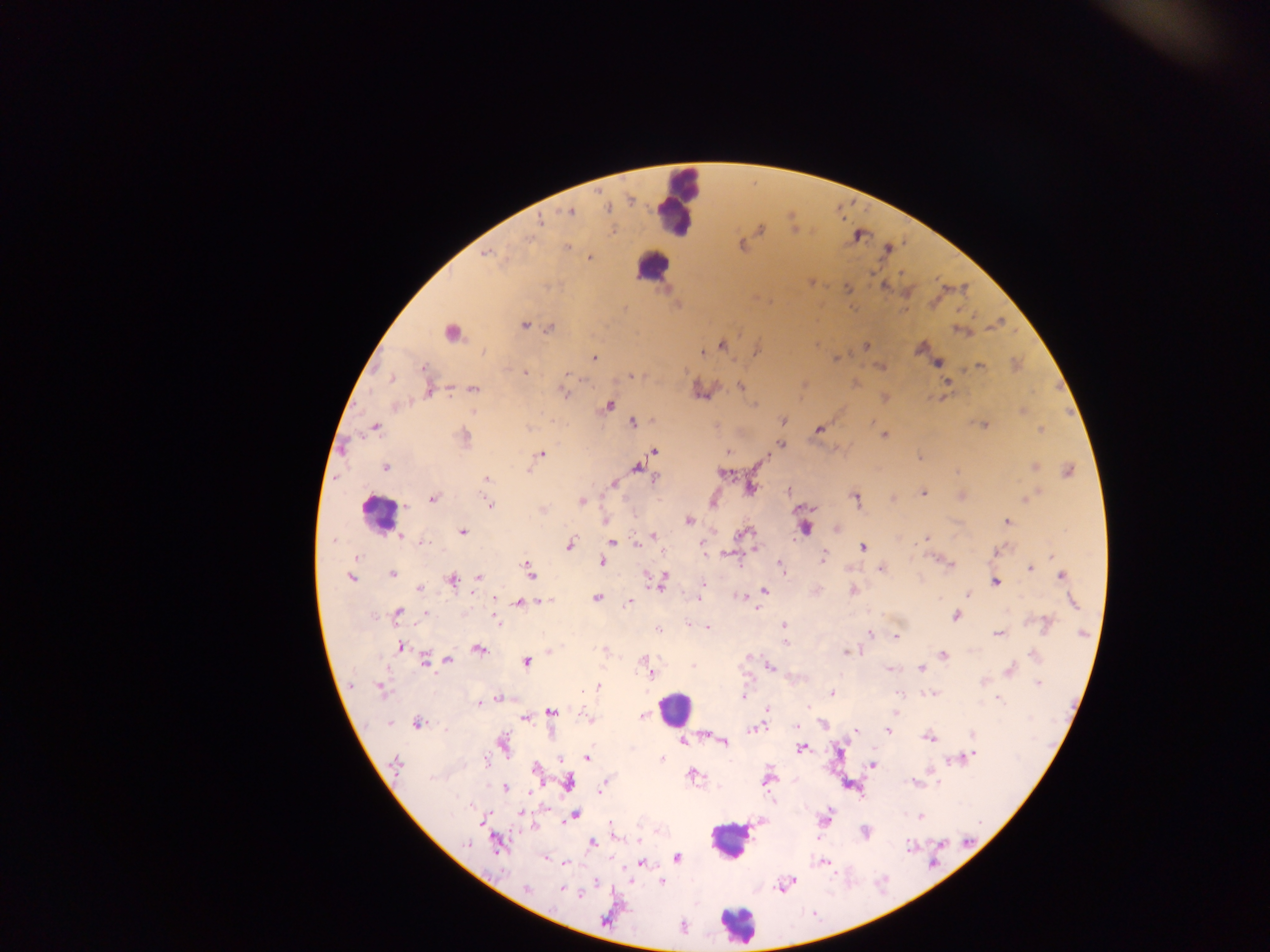
Approximate centers as [x, y] in pixels.
Summary:
  - Malaria parasite locations: [569, 212], [540, 220], [759, 229], [613, 230], [741, 245], [567, 247], [487, 255], [589, 258], [810, 282], [883, 285], [847, 288], [963, 289], [524, 325], [995, 325], [549, 328], [961, 331], [452, 332], [721, 344], [866, 346], [920, 347], [756, 351], [700, 353], [593, 358], [835, 358], [937, 363], [1014, 365], [880, 366], [979, 367], [524, 373], [630, 375], [391, 378], [804, 384], [854, 384], [947, 384], [741, 386], [428, 388], [473, 389], [563, 392], [884, 398], [397, 405], [608, 406], [1022, 410], [782, 421], [633, 422], [983, 425], [374, 426], [818, 430], [1040, 430], [884, 435], [463, 438], [780, 445], [652, 450], [727, 451], [540, 454], [920, 456], [645, 458], [1033, 466], [386, 467], [636, 467], [528, 470], [1068, 471], [723, 473], [486, 479], [655, 479], [613, 483], [749, 488], [789, 490], [922, 492], [962, 496], [855, 497], [432, 498], [892, 498], [1026, 498], [581, 501], [711, 501], [488, 504], [542, 510], [606, 519], [687, 520], [1006, 522], [804, 526], [837, 528], [462, 532], [744, 532], [654, 536], [399, 537], [926, 537], [612, 542], [423, 543], [569, 544], [637, 544], [703, 546], [862, 547], [996, 550], [729, 553], [822, 557], [1051, 557], [355, 558], [942, 561], [602, 562], [780, 568], [881, 568], [1029, 568], [529, 570], [392, 574], [1061, 575], [351, 577], [479, 577], [648, 577], [451, 580], [662, 580], [995, 581], [703, 583], [418, 588], [764, 590], [853, 590], [968, 593], [741, 596], [597, 598], [495, 599], [698, 599], [542, 600], [628, 601], [519, 602], [1072, 602], [759, 608], [397, 613], [425, 614], [955, 615], [495, 617], [1046, 623], [688, 624], [782, 624], [657, 629], [708, 629], [869, 633], [998, 633], [895, 637], [785, 642], [399, 646], [478, 649], [605, 650], [549, 651], [846, 651], [943, 654], [446, 659], [426, 660], [526, 662], [646, 663], [769, 666], [920, 668], [889, 669], [1009, 669], [651, 673], [1038, 683], [598, 687], [380, 689], [830, 692], [930, 693], [742, 697], [996, 697], [499, 699], [489, 701], [480, 702], [766, 709], [894, 711], [551, 712], [641, 716], [524, 718], [589, 719], [417, 724], [823, 724], [796, 726], [755, 728], [887, 731], [972, 733], [704, 734], [929, 737], [683, 741], [722, 741], [501, 745], [801, 747], [586, 757], [965, 757], [662, 758], [872, 764], [396, 765], [535, 769], [692, 775], [767, 778], [914, 782], [568, 783], [937, 783], [602, 785], [503, 787], [520, 813], [574, 814], [919, 816], [824, 819], [482, 822], [864, 831], [613, 835], [592, 842], [496, 843], [676, 857], [564, 862], [641, 862], [823, 862], [661, 881], [595, 882], [785, 883], [561, 888], [526, 890], [581, 893], [605, 920], [683, 926]
  - Leukocyte locations: [678, 200], [653, 265], [378, 513], [674, 709], [729, 840], [737, 925]
  - Capture: mobile-phone photograph through a microscope
  - Field of view: single
  - Image size: 1270×952 pixels
  - Preparation: thick blood film
  - Country: Ghana